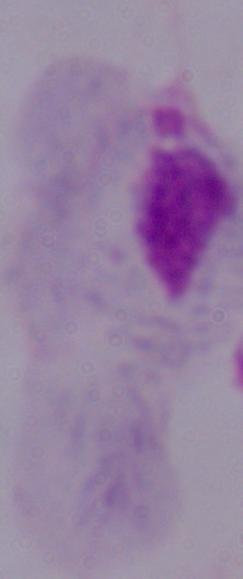

{
  "identification": "trichomonad",
  "magnification": "1000x",
  "modality": "photomicrograph"
}